Locate the cells, classifying each as a parasitized RBC, an uninfected RBC, or a WBC.
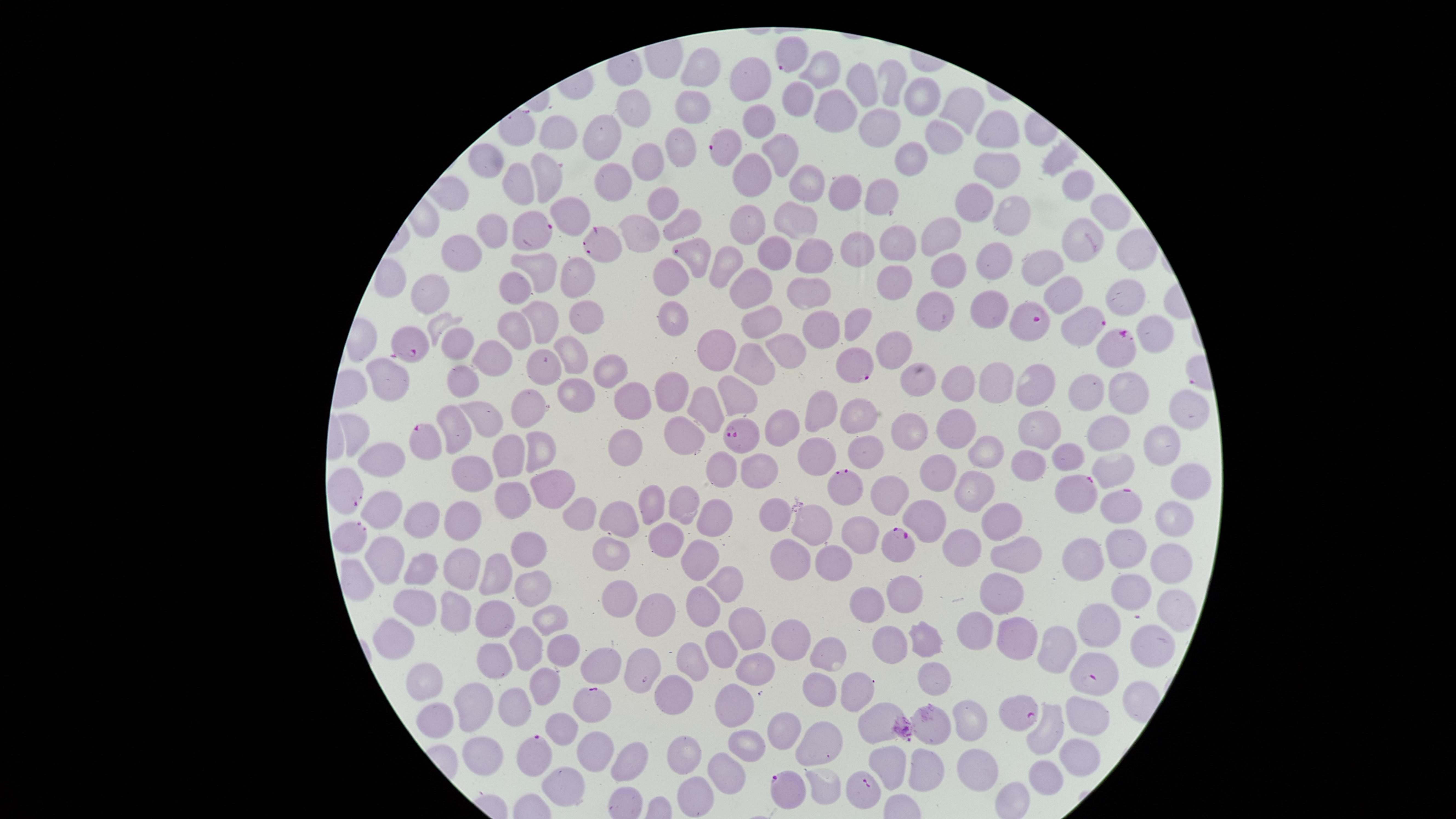

Approximate marker points, in pixels from the top-left corner.
Parasitized RBCs: (x=789, y=53), (x=729, y=148), (x=535, y=229), (x=598, y=244), (x=690, y=254), (x=1081, y=322), (x=1026, y=326), (x=1121, y=343), (x=410, y=348), (x=853, y=366), (x=744, y=436), (x=420, y=439), (x=837, y=487), (x=348, y=490), (x=1077, y=493), (x=1123, y=506), (x=353, y=537), (x=896, y=547), (x=1099, y=677), (x=590, y=701), (x=1022, y=711), (x=537, y=758), (x=866, y=789), (x=784, y=792).
Uninfected RBCs: (x=705, y=68), (x=823, y=70), (x=751, y=75), (x=892, y=81), (x=862, y=86), (x=915, y=96), (x=800, y=98), (x=646, y=106), (x=830, y=108), (x=960, y=109), (x=688, y=114), (x=754, y=123), (x=879, y=124), (x=999, y=130), (x=602, y=134), (x=551, y=135), (x=941, y=138), (x=680, y=157), (x=780, y=157), (x=904, y=158), (x=647, y=160), (x=997, y=164), (x=491, y=169), (x=546, y=173), (x=747, y=178), (x=606, y=179), (x=808, y=183), (x=1075, y=185), (x=521, y=187), (x=843, y=187), (x=879, y=193), (x=660, y=200), (x=974, y=202), (x=1118, y=209), (x=1007, y=211), (x=569, y=216), (x=786, y=220), (x=680, y=221), (x=747, y=226), (x=641, y=227), (x=489, y=234), (x=942, y=234), (x=1080, y=237), (x=895, y=239), (x=849, y=248), (x=1133, y=248), (x=462, y=251), (x=778, y=251), (x=810, y=255), (x=728, y=258), (x=990, y=258), (x=537, y=265), (x=1032, y=266), (x=948, y=267), (x=671, y=274), (x=577, y=278), (x=889, y=284), (x=515, y=285), (x=742, y=285), (x=806, y=290), (x=427, y=291), (x=1062, y=295), (x=1126, y=295), (x=934, y=301), (x=985, y=310), (x=672, y=313), (x=589, y=317), (x=852, y=318), (x=540, y=321), (x=764, y=325), (x=828, y=325), (x=518, y=327), (x=1152, y=338), (x=454, y=345), (x=890, y=349), (x=576, y=350), (x=715, y=352), (x=793, y=352), (x=488, y=357), (x=754, y=363), (x=537, y=366), (x=605, y=370), (x=919, y=375), (x=1039, y=380), (x=961, y=381), (x=1003, y=381), (x=462, y=383), (x=390, y=384), (x=1089, y=386), (x=571, y=391), (x=670, y=391), (x=1134, y=391), (x=731, y=392), (x=637, y=398), (x=709, y=403), (x=819, y=403), (x=532, y=408), (x=1181, y=410), (x=854, y=415), (x=483, y=422), (x=952, y=424), (x=910, y=426), (x=456, y=427), (x=1031, y=427), (x=785, y=430), (x=356, y=432), (x=684, y=433), (x=1108, y=437), (x=622, y=443), (x=1165, y=445), (x=868, y=447), (x=537, y=450), (x=517, y=452), (x=817, y=452), (x=985, y=454), (x=1063, y=459), (x=1110, y=460), (x=386, y=462), (x=1023, y=464), (x=762, y=471), (x=476, y=472), (x=1188, y=473), (x=947, y=474), (x=716, y=477), (x=553, y=479), (x=971, y=484), (x=890, y=491), (x=513, y=492), (x=681, y=502), (x=645, y=506), (x=576, y=508), (x=389, y=510), (x=778, y=511), (x=714, y=516), (x=1007, y=517), (x=1176, y=517), (x=928, y=518), (x=425, y=519), (x=813, y=519), (x=463, y=520), (x=617, y=521), (x=851, y=528), (x=666, y=535), (x=961, y=544), (x=1126, y=547), (x=534, y=549), (x=789, y=550), (x=607, y=552), (x=698, y=557), (x=1088, y=557), (x=832, y=559), (x=1014, y=559), (x=1168, y=562), (x=388, y=563), (x=425, y=568), (x=458, y=574), (x=504, y=574), (x=724, y=582), (x=532, y=587), (x=1131, y=593), (x=907, y=594), (x=618, y=597), (x=411, y=601), (x=708, y=601), (x=863, y=601), (x=1000, y=601), (x=655, y=608), (x=453, y=609), (x=495, y=610), (x=547, y=616), (x=1173, y=616), (x=1100, y=621), (x=745, y=622), (x=927, y=627), (x=979, y=630), (x=1018, y=634), (x=789, y=638), (x=528, y=639), (x=892, y=639), (x=397, y=640), (x=724, y=641), (x=1149, y=643), (x=1055, y=646), (x=563, y=647), (x=500, y=653), (x=826, y=655), (x=692, y=657), (x=599, y=665), (x=638, y=665), (x=762, y=666), (x=930, y=670), (x=817, y=678), (x=429, y=679), (x=544, y=685), (x=851, y=687), (x=673, y=692), (x=478, y=699), (x=514, y=708), (x=731, y=709), (x=436, y=711), (x=1077, y=716), (x=881, y=718), (x=971, y=721), (x=1046, y=724), (x=781, y=725), (x=748, y=741), (x=689, y=743), (x=825, y=743), (x=480, y=753), (x=1075, y=757), (x=887, y=762), (x=919, y=766), (x=640, y=768), (x=726, y=768), (x=983, y=768), (x=1040, y=778), (x=825, y=788), (x=690, y=793).
No WBCs identified.

Species: Plasmodium falciparum. Single field of view. Image is 1456×819 pixels. Smartphone photograph through the microscope eyepiece. Giemsa-stained preparation. The visible region is circular. Thin blood film.